Give the extent of all uninfected red blood cells.
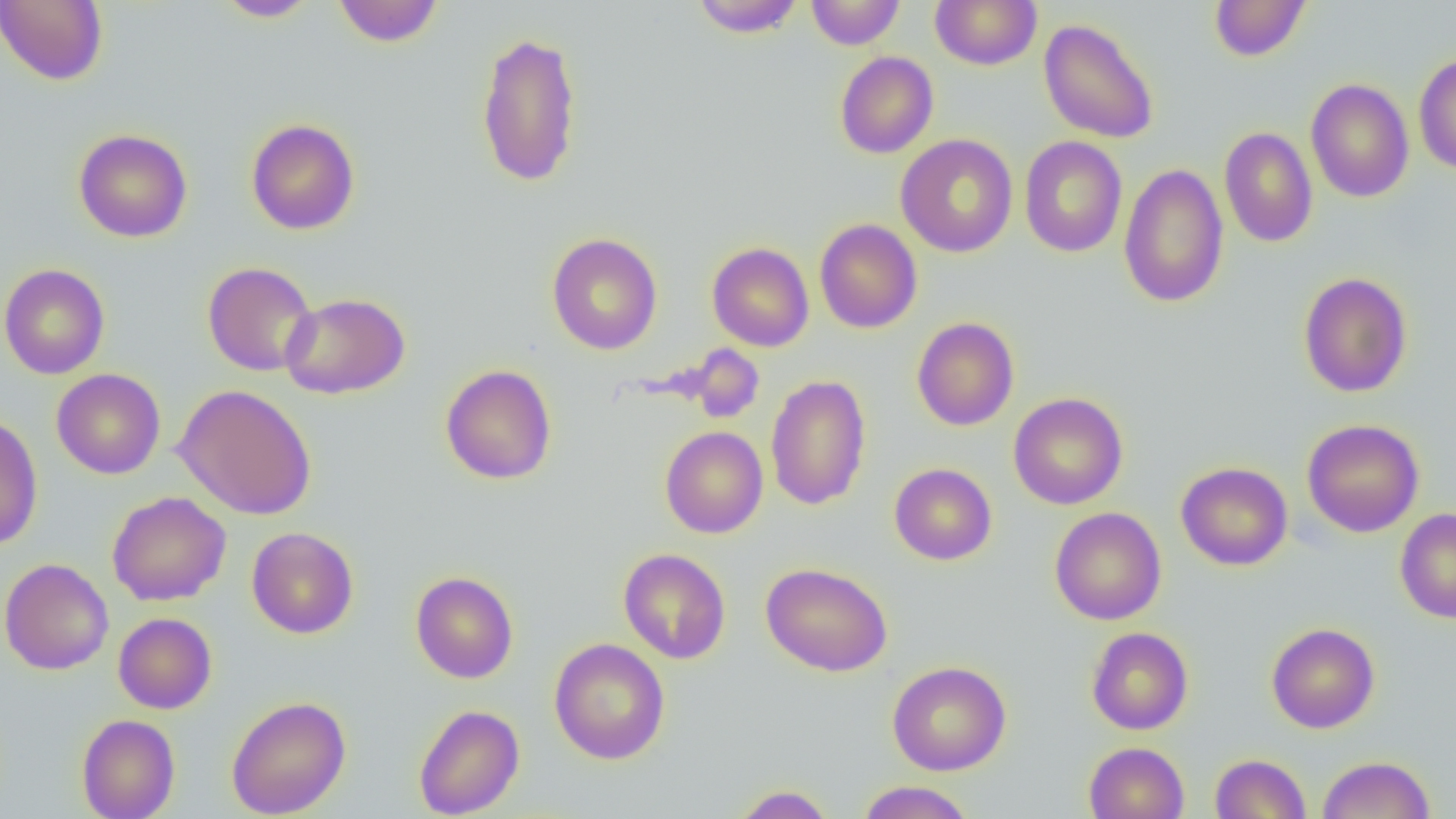
Approximate bounding boxes as (x1,y1)-(x2,y2) corner pairs in pixels.
Uninfected red blood cells: (0,0)-(108,86), (215,0)-(320,22), (332,0)-(444,47), (691,0)-(804,37), (805,0)-(905,49), (930,0)-(1042,70), (1209,0)-(1312,62), (1038,17)-(1159,144), (475,30)-(583,188), (835,51)-(938,159), (1413,54)-(1456,174), (1305,78)-(1414,203), (245,118)-(360,235), (1219,126)-(1319,248), (74,129)-(192,243), (895,134)-(1018,258), (1019,136)-(1127,258), (1119,163)-(1229,309), (814,218)-(922,334), (547,232)-(663,355), (707,242)-(814,352), (202,261)-(318,376), (0,263)-(110,380), (1298,271)-(1413,398), (280,292)-(410,399), (911,317)-(1020,431), (685,345)-(765,423), (440,364)-(557,485), (51,368)-(166,479), (765,374)-(872,511), (173,384)-(317,520), (1008,392)-(1128,510), (0,413)-(43,551), (1302,419)-(1424,537), (660,426)-(768,538), (1176,461)-(1293,570), (889,463)-(997,565), (106,491)-(231,606), (1049,507)-(1166,625), (1395,508)-(1456,623), (246,526)-(359,639), (618,547)-(731,664), (0,558)-(114,675), (760,562)-(893,677), (410,571)-(518,683), (113,612)-(217,714), (1267,622)-(1380,733), (1086,627)-(1194,735), (549,638)-(670,764), (887,661)-(1011,776), (226,695)-(351,818), (414,704)-(525,818), (76,713)-(180,819), (1083,741)-(1189,819), (1210,753)-(1311,818), (1317,755)-(1435,819), (856,781)-(976,818), (729,784)-(837,818).

Slide-level diagnosis: no evidence of blood parasites. Light microscopy. Image is 1456×819 pixels. Thin blood film. 1000x magnification. One field of a larger specimen.